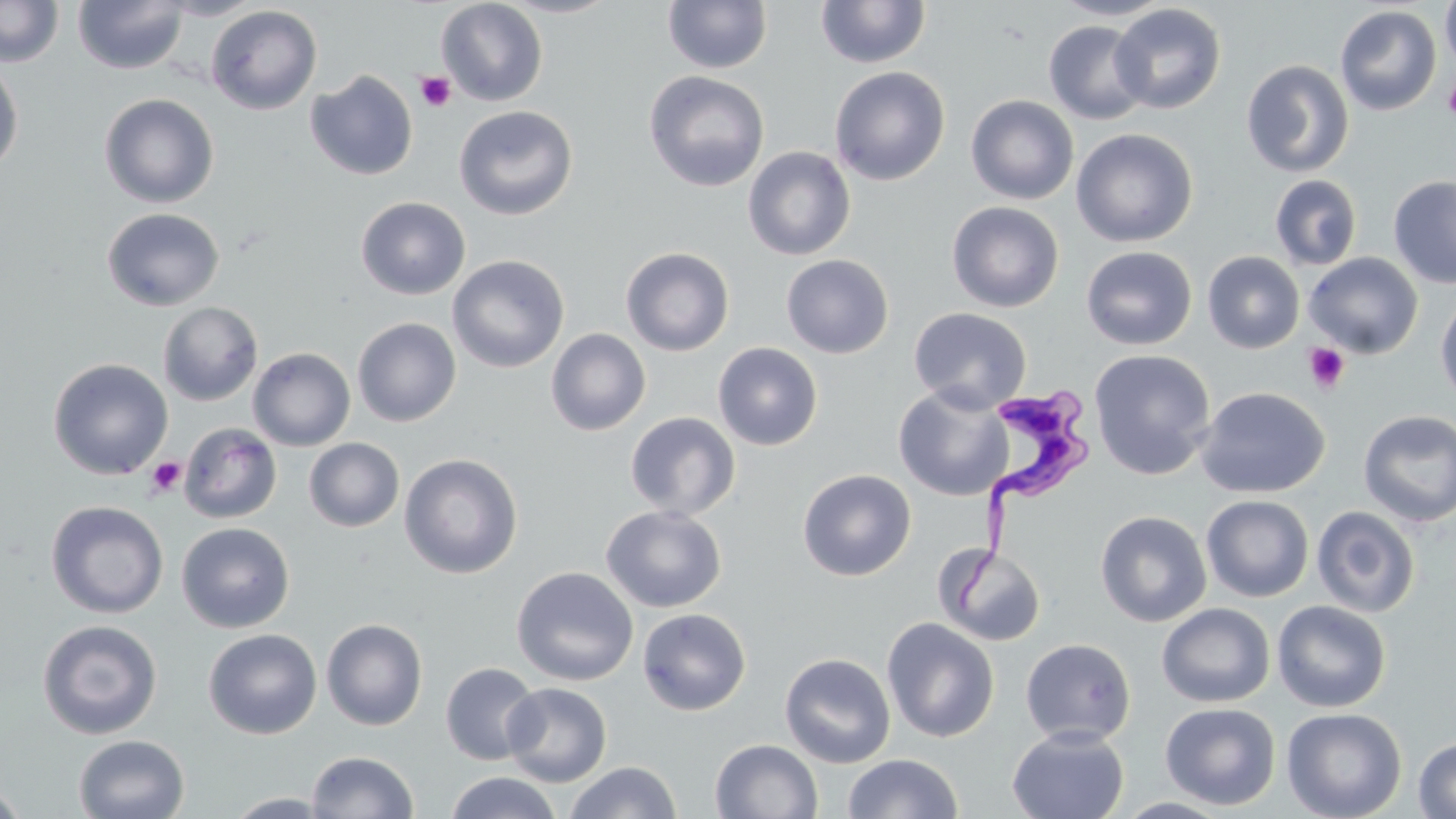
Trypanosoma brucei locations = approximate bounding boxes as (x1,y1)-(x2,y2) corner pairs in pixels: (953,385)-(1099,615)
slide-level diagnosis = Trypanosoma brucei
uninfected red blood cell locations = approximate bounding boxes as (x1,y1)-(x2,y2) corner pairs in pixels: (0,0)-(64,67), (155,0)-(267,20), (436,0)-(548,106), (496,0)-(622,19), (662,0)-(773,73), (1050,0)-(1176,21), (73,1)-(189,74), (816,1)-(931,69), (1440,1)-(1456,72), (1109,3)-(1227,114), (206,5)-(322,115), (1335,5)-(1442,116), (1043,20)-(1151,125), (0,56)-(24,177), (1241,59)-(1354,178), (829,65)-(950,186), (305,70)-(418,181), (643,70)-(770,192), (99,93)-(220,208), (966,95)-(1079,205), (454,105)-(578,221), (1071,128)-(1198,247), (742,146)-(856,261), (1270,174)-(1362,271), (1388,175)-(1456,289), (355,196)-(471,300), (947,201)-(1064,312), (101,207)-(225,311), (1080,245)-(1198,350), (621,247)-(734,356), (1202,251)-(1305,354), (1303,252)-(1423,358), (781,254)-(894,358), (447,255)-(569,374), (1435,292)-(1456,408), (158,302)-(263,406), (908,306)-(1032,413), (352,317)-(461,427), (545,328)-(651,436), (713,341)-(823,451), (248,347)-(356,451), (1089,349)-(1216,479), (48,358)-(173,480), (893,384)-(1013,501), (1195,386)-(1330,498), (1358,410)-(1456,527), (625,411)-(740,520), (178,422)-(283,523), (304,438)-(404,532), (399,453)-(523,579), (797,468)-(917,581), (1201,495)-(1314,602), (46,500)-(168,618), (601,505)-(726,613), (1311,506)-(1421,618), (1095,510)-(1212,627), (176,522)-(295,633), (933,543)-(1047,647), (511,566)-(638,686), (1272,600)-(1392,712), (1157,603)-(1275,707), (637,607)-(751,716), (881,617)-(1000,742), (321,618)-(428,731), (37,619)-(162,740), (203,628)-(323,740), (1020,638)-(1136,746), (780,652)-(896,768), (440,662)-(542,765), (502,682)-(612,787), (1160,702)-(1281,810), (1281,707)-(1407,819), (1006,726)-(1130,819), (73,734)-(190,819), (1414,736)-(1456,818), (710,738)-(823,819), (306,750)-(419,818), (842,753)-(963,818), (564,761)-(682,819), (444,771)-(563,819), (0,782)-(29,819), (223,792)-(338,818)
image size = 1456×819 pixels
magnification = 1000x
preparation = thin blood smear
modality = light microscopy
stain = May-Grünwald-Giemsa
field of view = one of a larger specimen
platelet locations = approximate bounding boxes as (x1,y1)-(x2,y2) corner pairs in pixels: (415,71)-(457,112), (1443,78)-(1456,121), (1302,342)-(1351,394), (146,457)-(186,496)